Report the malaria status of this cell.
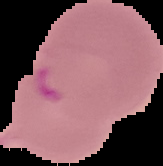

Parasitized.

Summary:
  - Image type: cell region segmented out of the field of view; surrounding area masked to black
  - Image size: 163×166 pixels
  - Preparation: thin blood smear